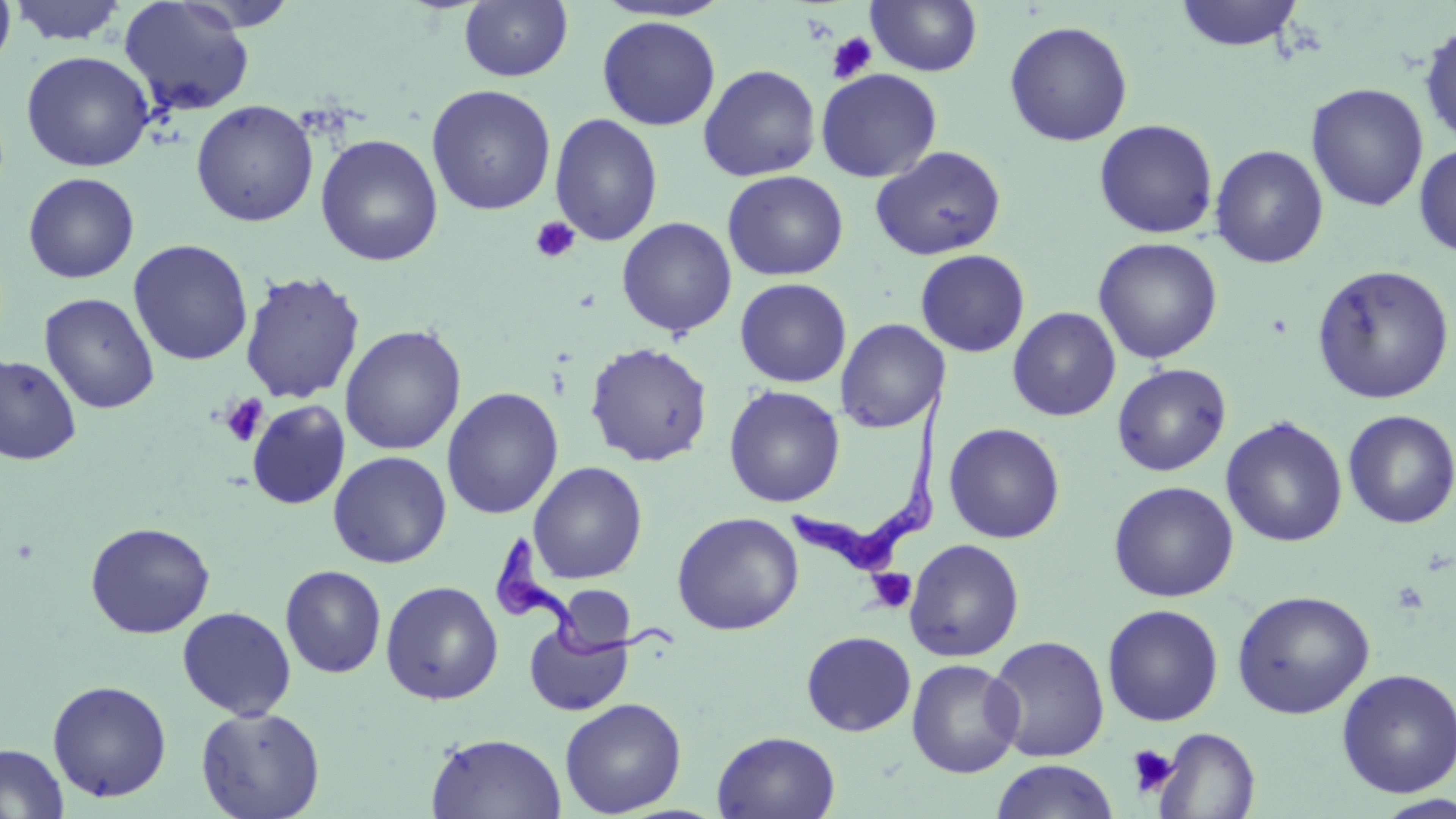
slide-level diagnosis = Trypanosoma brucei
preparation = thin blood film
uninfected red blood cell locations = approximate bounding boxes as (x1,y1)-(x2,y2) corner pairs in pixels: (0,0)-(17,75), (118,0)-(255,117), (459,0)-(573,82), (866,0)-(983,76), (1175,0)-(1303,52), (7,1)-(129,46), (597,15)-(721,131), (1003,20)-(1133,147), (1418,21)-(1456,148), (21,51)-(155,172), (698,64)-(821,181), (815,68)-(942,183), (1305,82)-(1430,212), (426,84)-(557,216), (191,100)-(319,227), (549,112)-(663,246), (1094,118)-(1219,239), (315,134)-(443,267), (1414,142)-(1456,257), (1209,144)-(1329,269), (870,145)-(1006,260), (722,170)-(848,281), (23,172)-(140,284), (616,217)-(738,338), (1092,236)-(1223,364), (128,239)-(253,365), (915,250)-(1030,357), (1311,264)-(1454,404), (239,270)-(365,404), (735,278)-(851,387), (40,293)-(159,414), (1007,306)-(1121,421), (835,318)-(949,433), (339,324)-(466,456), (584,342)-(713,467), (0,354)-(81,465), (1111,362)-(1231,477), (724,385)-(845,507), (442,387)-(563,519), (246,400)-(350,510), (1342,409)-(1456,529), (1221,416)-(1348,548), (943,422)-(1065,544), (328,451)-(451,569), (528,461)-(648,584), (1108,480)-(1239,602), (671,512)-(804,636), (85,521)-(216,638), (903,538)-(1024,662), (280,565)-(386,679), (380,580)-(504,705), (556,584)-(638,652), (1231,589)-(1375,719), (1102,604)-(1224,726), (177,606)-(296,720), (524,624)-(634,716), (801,630)-(917,736), (985,635)-(1111,763), (906,659)-(1023,778), (1336,668)-(1456,798), (47,679)-(172,802), (559,697)-(686,817), (195,705)-(326,819), (1154,727)-(1260,818), (712,731)-(841,818), (425,732)-(567,819), (0,743)-(68,819), (990,759)-(1119,819), (1376,795)-(1456,818)
modality = optical microscopy
magnification = 1000x
image size = 1456×819 pixels
field of view = single
Trypanosoma brucei locations = approximate bounding boxes as (x1,y1)-(x2,y2) corner pairs in pixels: (787,385)-(951,575), (488,530)-(681,661)
platelet locations = approximate bounding boxes as (x1,y1)-(x2,y2) corner pairs in pixels: (826,31)-(878,84), (529,216)-(582,264), (220,394)-(268,447), (866,569)-(917,614), (1127,745)-(1180,798)
stain = May-Grünwald-Giemsa